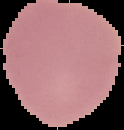
Summary:
  - Malaria status: uninfected
  - Image size: 124×130 pixels
  - Image type: segmented cell region on a black background
  - Preparation: thin blood smear